Outline each Plasmodium falciparum-infected red blood cell.
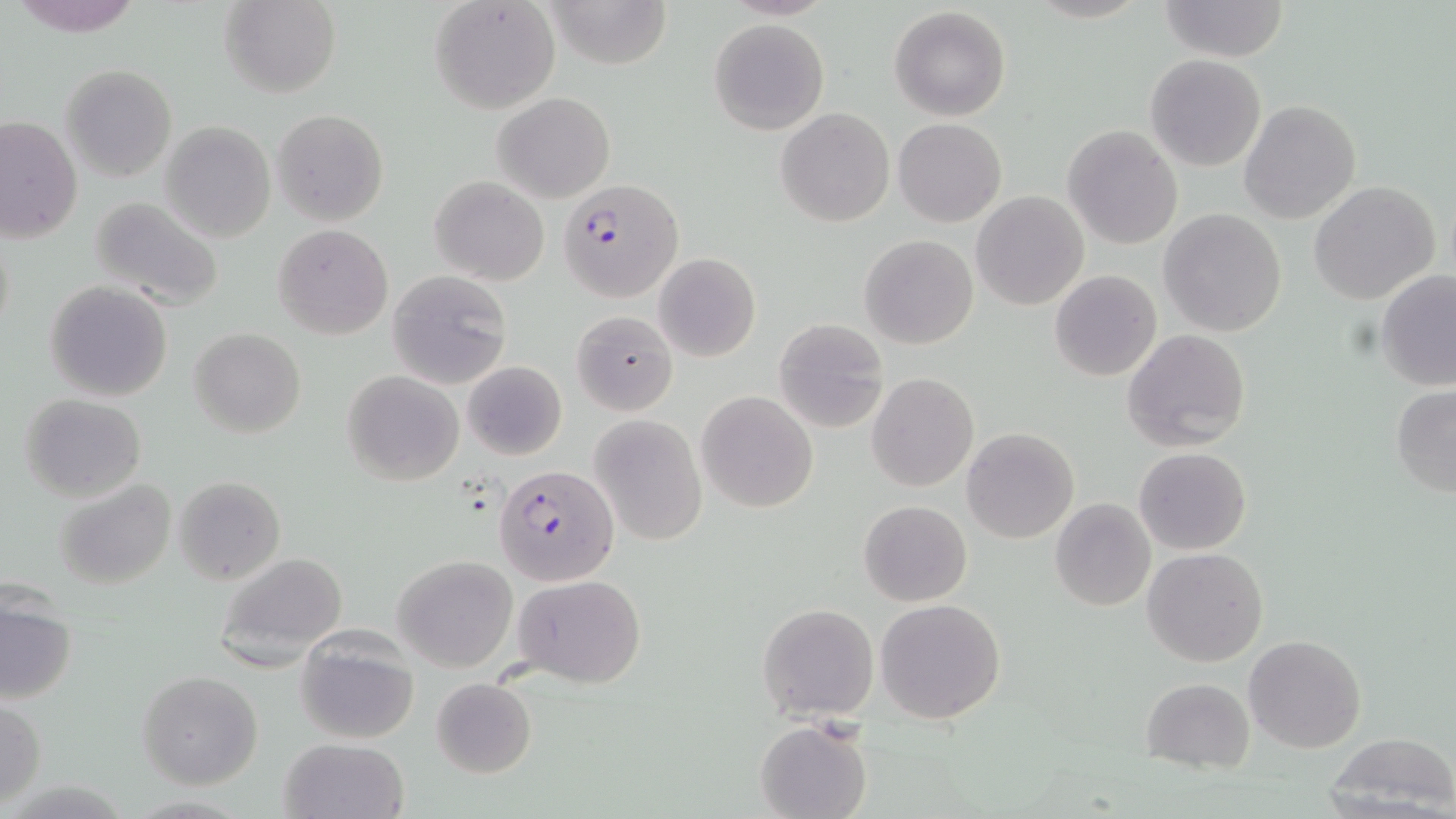
Approximate bounding boxes as (x1, y1, x2, y2) in pixels.
Plasmodium falciparum-infected red blood cells: (561, 178, 682, 302), (494, 464, 619, 597).

Uninfected red blood cell locations: (220, 0, 341, 98), (429, 0, 561, 115), (543, 0, 670, 70), (1157, 1, 1287, 60), (889, 6, 1011, 121), (708, 18, 829, 134), (1145, 54, 1267, 171), (61, 64, 176, 182), (493, 92, 614, 203), (1240, 100, 1360, 223), (272, 108, 389, 228), (776, 108, 893, 227), (1, 116, 82, 244), (893, 118, 1006, 227), (161, 120, 276, 243), (1063, 126, 1182, 249), (430, 175, 550, 285), (1309, 180, 1441, 305), (972, 192, 1089, 310), (89, 197, 226, 310), (1159, 208, 1288, 337), (1, 224, 15, 347), (273, 224, 394, 339), (860, 234, 978, 349), (653, 253, 761, 363), (1049, 269, 1162, 382), (387, 270, 512, 388), (1376, 270, 1456, 390), (46, 281, 173, 402), (572, 310, 677, 415), (773, 319, 888, 434), (189, 327, 306, 437), (1122, 328, 1251, 452), (462, 360, 566, 461), (341, 370, 465, 486), (866, 373, 978, 492), (1391, 386, 1456, 498), (696, 391, 818, 512), (19, 394, 146, 502), (588, 414, 706, 548), (963, 427, 1079, 544), (1134, 447, 1252, 555), (174, 476, 284, 585), (57, 479, 176, 589), (1050, 498, 1156, 611), (859, 500, 972, 605), (1142, 547, 1268, 668), (213, 551, 348, 669), (393, 555, 518, 672), (511, 574, 648, 687), (1, 596, 77, 705), (875, 598, 1006, 724), (757, 603, 878, 721), (294, 632, 419, 744), (1244, 634, 1367, 754), (138, 672, 262, 790), (431, 676, 537, 778), (1141, 677, 1254, 774), (0, 697, 45, 807), (755, 718, 872, 819), (1321, 732, 1456, 815), (281, 737, 409, 819). Slide-level diagnosis: Plasmodium falciparum. Thin blood smear. Image is 1456×819 pixels. May-Grünwald-Giemsa stain. 1000x magnification. Light microscopy. One field of a larger specimen.